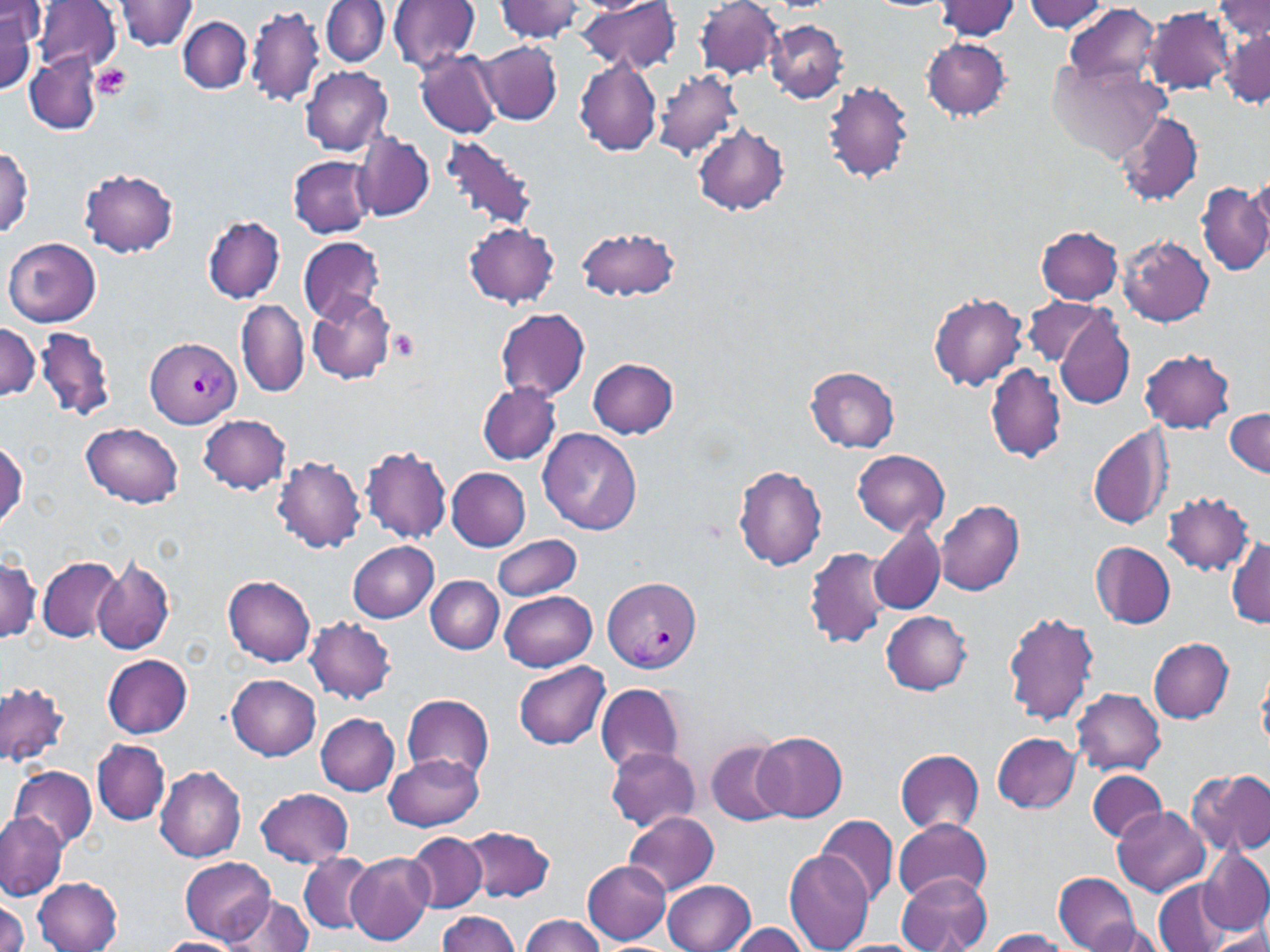

slide_level_diagnosis: Plasmodium vivax
preparation: thin blood smear
modality: optical microscopy
magnification: 1000x
uninfected_red_blood_cell_locations: 'approximate bounding boxes as named x1/y1/x2/y2 corners in pixels: (x1=117, y1=0, x2=198, y2=51), (x1=389, y1=0, x2=481, y2=72), (x1=494, y1=0, x2=587, y2=42), (x1=577, y1=0, x2=681, y2=74), (x1=695, y1=0, x2=783, y2=79), (x1=1213, y1=0, x2=1269, y2=45), (x1=34, y1=1, x2=121, y2=77), (x1=321, y1=1, x2=389, y2=67), (x1=935, y1=1, x2=1021, y2=40), (x1=1022, y1=1, x2=1112, y2=34), (x1=1063, y1=3, x2=1162, y2=89), (x1=244, y1=4, x2=324, y2=108), (x1=1145, y1=7, x2=1234, y2=94), (x1=0, y1=8, x2=35, y2=93), (x1=179, y1=16, x2=252, y2=95), (x1=766, y1=20, x2=847, y2=102), (x1=1219, y1=22, x2=1269, y2=111), (x1=920, y1=37, x2=1013, y2=121), (x1=478, y1=40, x2=561, y2=125), (x1=416, y1=50, x2=501, y2=137), (x1=24, y1=57, x2=101, y2=130), (x1=573, y1=59, x2=663, y2=155), (x1=1048, y1=61, x2=1170, y2=163), (x1=301, y1=65, x2=392, y2=155), (x1=654, y1=68, x2=743, y2=161), (x1=821, y1=82, x2=915, y2=183), (x1=1117, y1=112, x2=1202, y2=206), (x1=692, y1=123, x2=789, y2=215), (x1=354, y1=133, x2=434, y2=222), (x1=442, y1=134, x2=540, y2=233), (x1=0, y1=146, x2=34, y2=240), (x1=288, y1=155, x2=377, y2=238), (x1=79, y1=168, x2=179, y2=258), (x1=1242, y1=174, x2=1270, y2=260), (x1=1196, y1=182, x2=1269, y2=277), (x1=202, y1=215, x2=286, y2=303), (x1=463, y1=221, x2=561, y2=307), (x1=577, y1=225, x2=682, y2=302), (x1=1036, y1=226, x2=1124, y2=304), (x1=1118, y1=235, x2=1214, y2=327), (x1=297, y1=236, x2=386, y2=324), (x1=4, y1=237, x2=102, y2=327), (x1=929, y1=291, x2=1027, y2=389), (x1=307, y1=294, x2=397, y2=385), (x1=1023, y1=295, x2=1110, y2=370), (x1=236, y1=299, x2=309, y2=398), (x1=1054, y1=306, x2=1134, y2=411), (x1=496, y1=307, x2=592, y2=401), (x1=0, y1=321, x2=41, y2=403), (x1=34, y1=326, x2=116, y2=422), (x1=1139, y1=349, x2=1235, y2=433), (x1=588, y1=358, x2=678, y2=437), (x1=985, y1=362, x2=1067, y2=464), (x1=806, y1=367, x2=900, y2=452), (x1=477, y1=383, x2=562, y2=464), (x1=1225, y1=409, x2=1270, y2=475), (x1=199, y1=414, x2=292, y2=494), (x1=83, y1=422, x2=184, y2=508), (x1=1089, y1=422, x2=1174, y2=531), (x1=538, y1=429, x2=642, y2=535), (x1=0, y1=438, x2=26, y2=531), (x1=360, y1=445, x2=453, y2=546), (x1=852, y1=449, x2=950, y2=535), (x1=271, y1=457, x2=367, y2=553), (x1=734, y1=465, x2=828, y2=571), (x1=447, y1=467, x2=530, y2=551), (x1=1162, y1=492, x2=1255, y2=575), (x1=936, y1=499, x2=1025, y2=595), (x1=870, y1=520, x2=946, y2=614), (x1=492, y1=535, x2=581, y2=600), (x1=1227, y1=535, x2=1270, y2=627), (x1=347, y1=540, x2=439, y2=622), (x1=1089, y1=541, x2=1175, y2=628), (x1=804, y1=547, x2=890, y2=649), (x1=0, y1=553, x2=41, y2=643), (x1=37, y1=557, x2=121, y2=642), (x1=92, y1=557, x2=175, y2=655), (x1=223, y1=574, x2=316, y2=667), (x1=425, y1=576, x2=504, y2=653), (x1=499, y1=590, x2=597, y2=672), (x1=881, y1=610, x2=972, y2=695), (x1=1002, y1=610, x2=1098, y2=726), (x1=306, y1=617, x2=397, y2=703), (x1=1148, y1=637, x2=1233, y2=723), (x1=102, y1=654, x2=193, y2=738), (x1=515, y1=661, x2=611, y2=750), (x1=1257, y1=667, x2=1270, y2=752), (x1=227, y1=674, x2=321, y2=760), (x1=0, y1=680, x2=71, y2=768), (x1=595, y1=684, x2=686, y2=775), (x1=1072, y1=689, x2=1165, y2=775), (x1=401, y1=695, x2=495, y2=782), (x1=315, y1=712, x2=400, y2=796), (x1=754, y1=730, x2=847, y2=823), (x1=993, y1=731, x2=1081, y2=813), (x1=93, y1=739, x2=170, y2=825), (x1=702, y1=739, x2=788, y2=827), (x1=604, y1=746, x2=700, y2=832), (x1=895, y1=749, x2=985, y2=835), (x1=384, y1=752, x2=485, y2=831), (x1=11, y1=765, x2=98, y2=849), (x1=154, y1=766, x2=246, y2=862), (x1=1087, y1=769, x2=1167, y2=843), (x1=1187, y1=769, x2=1270, y2=856), (x1=255, y1=787, x2=353, y2=867), (x1=1114, y1=806, x2=1211, y2=896), (x1=622, y1=811, x2=720, y2=896), (x1=0, y1=812, x2=66, y2=899), (x1=816, y1=815, x2=898, y2=907), (x1=893, y1=817, x2=991, y2=904), (x1=462, y1=824, x2=558, y2=904), (x1=406, y1=831, x2=486, y2=912), (x1=784, y1=848, x2=873, y2=951), (x1=1198, y1=848, x2=1270, y2=934), (x1=299, y1=852, x2=373, y2=935), (x1=345, y1=853, x2=434, y2=944), (x1=180, y1=856, x2=277, y2=944), (x1=582, y1=857, x2=672, y2=944), (x1=1054, y1=872, x2=1140, y2=951), (x1=898, y1=874, x2=992, y2=952), (x1=33, y1=877, x2=123, y2=951), (x1=1154, y1=878, x2=1232, y2=952), (x1=662, y1=880, x2=756, y2=952), (x1=222, y1=894, x2=314, y2=952), (x1=0, y1=897, x2=26, y2=952), (x1=437, y1=912, x2=523, y2=951), (x1=520, y1=915, x2=607, y2=952), (x1=1086, y1=920, x2=1168, y2=952), (x1=724, y1=923, x2=811, y2=952), (x1=985, y1=927, x2=1072, y2=951), (x1=1206, y1=927, x2=1270, y2=950), (x1=157, y1=936, x2=245, y2=952)'
image_size: 1270×952 pixels
field_of_view: single
platelet_locations: 'approximate bounding boxes as named x1/y1/x2/y2 corners in pixels: (x1=92, y1=65, x2=131, y2=100), (x1=390, y1=329, x2=420, y2=360)'
stain: May-Grünwald-Giemsa
plasmodium_vivax_infected_red_blood_cell_locations: 'approximate bounding boxes as named x1/y1/x2/y2 corners in pixels: (x1=146, y1=338, x2=242, y2=428), (x1=603, y1=575, x2=700, y2=673)'